Assess the morphology of the red blood cells.
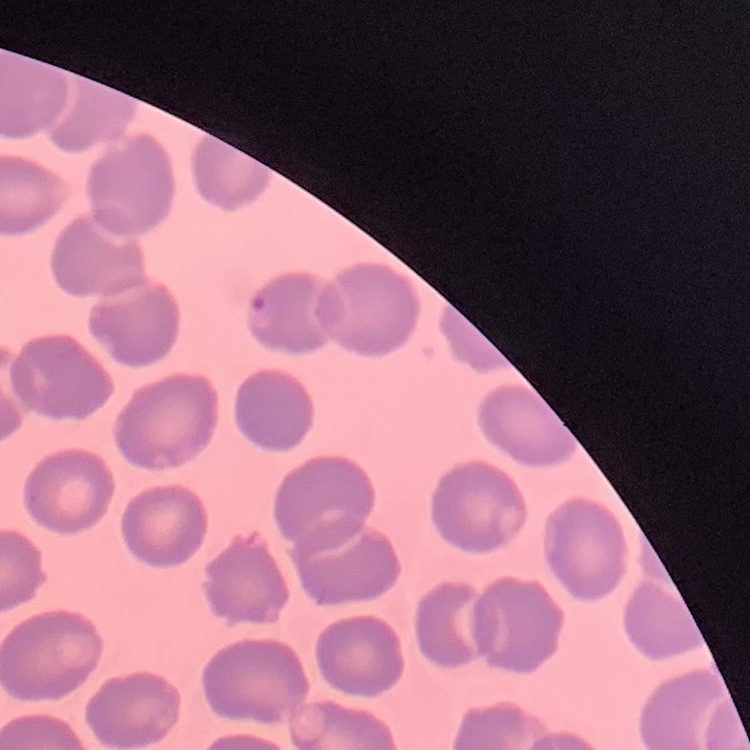

No rouleaux formation.

image type = square crop of a larger photomicrograph
preparation = thin blood film
stain = Field's or Giemsa